Comment on the morphology of the erythrocytes.
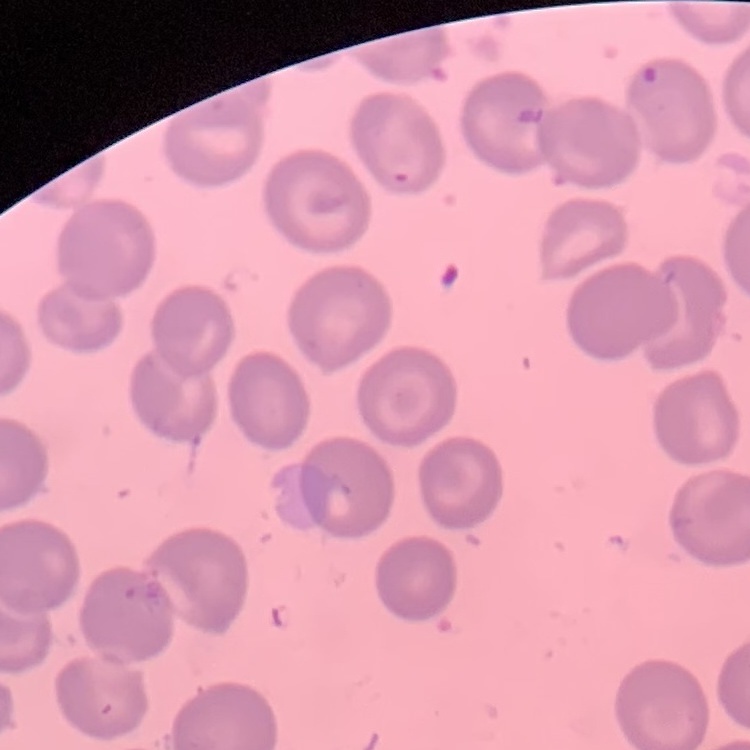
No rouleaux formation.

preparation: thin blood film
stain: Field's or Giemsa
image_type: one tile cut from a larger photomicrograph